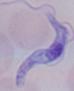

{
  "identification": "trypanosome",
  "modality": "photomicrograph",
  "magnification": "1000x"
}